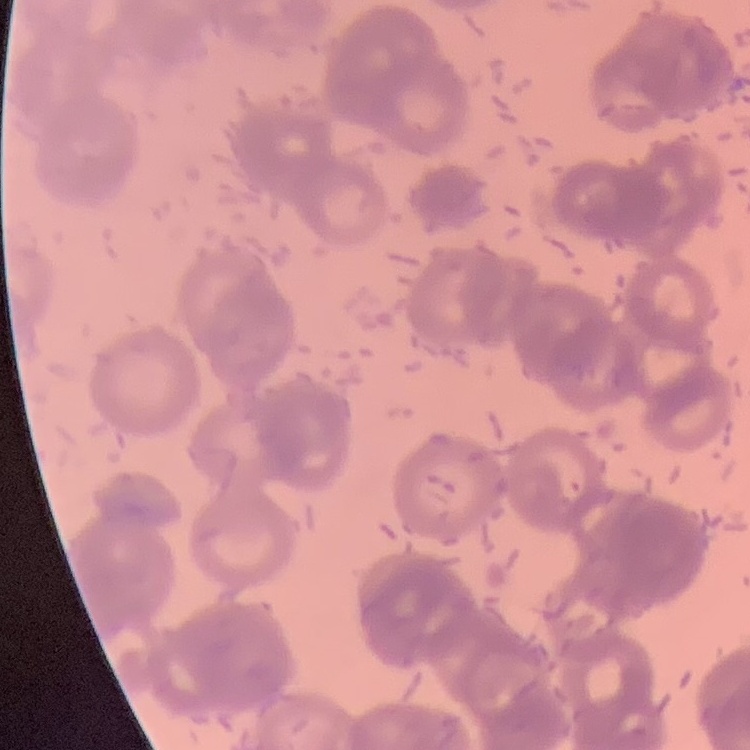
Summary:
  - Erythrocyte morphology: rouleaux formation
  - Preparation: thin blood film
  - Image type: square crop of a larger photomicrograph
  - Stain: Field's or Giemsa